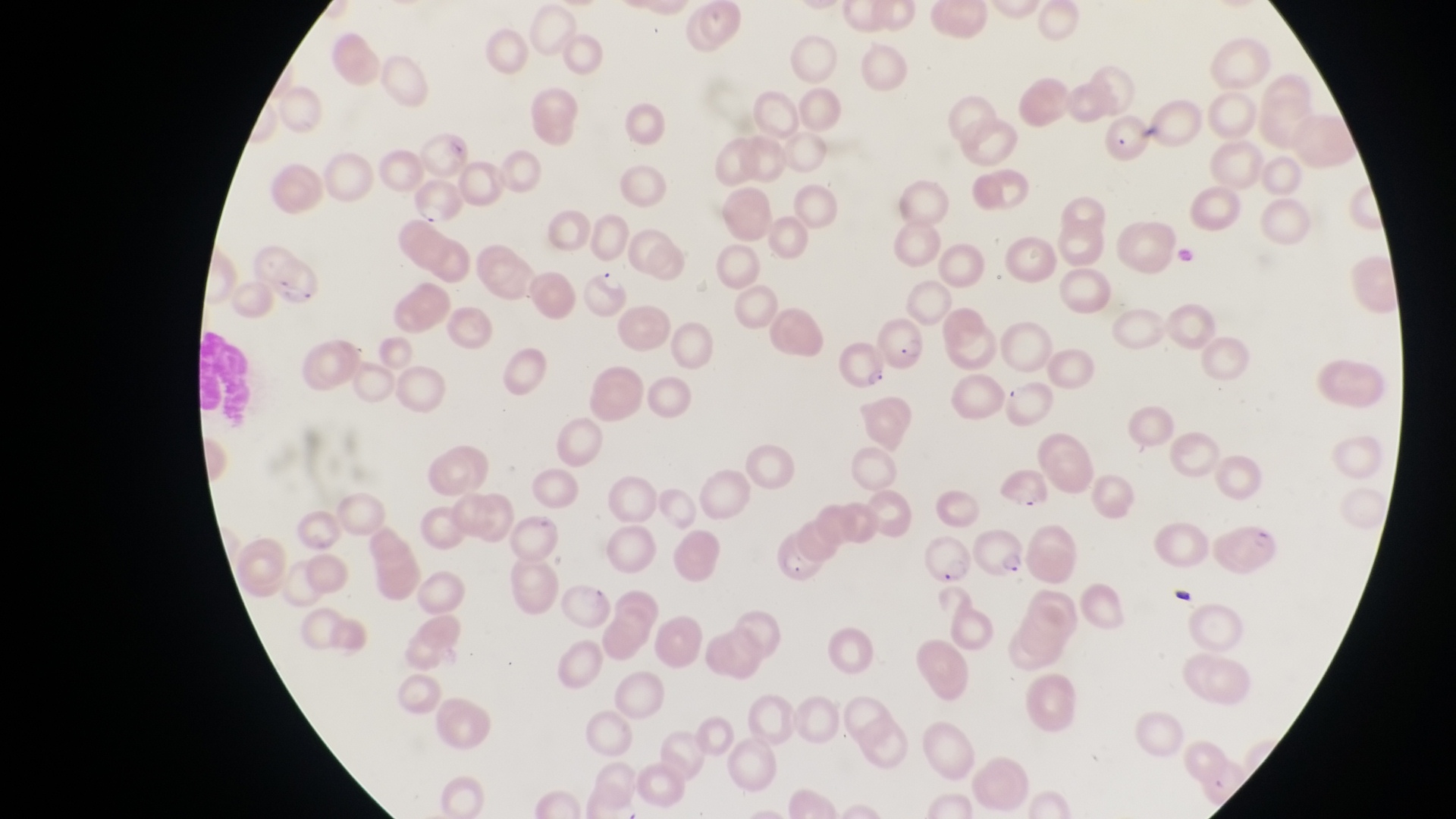
Approximate bounding boxes as [left, top, right, bottom] in pixels. Parasitised red blood cell locations: [415, 178, 464, 231], [579, 265, 631, 317], [874, 309, 929, 365], [833, 336, 893, 395], [971, 528, 1031, 581], [924, 531, 971, 587], [770, 535, 830, 582]. Photographed through the eyepiece of an Olympus CX-23 microscope with a smartphone camera. Thin blood smear. Image is 1456×819 pixels. Magnification of 1000x. Collected in Uganda. One field of view.